Classify this cell by malaria status.
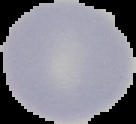
Uninfected.

preparation = thin blood film
image size = 136×124 pixels
image type = segmented cell region on a black background